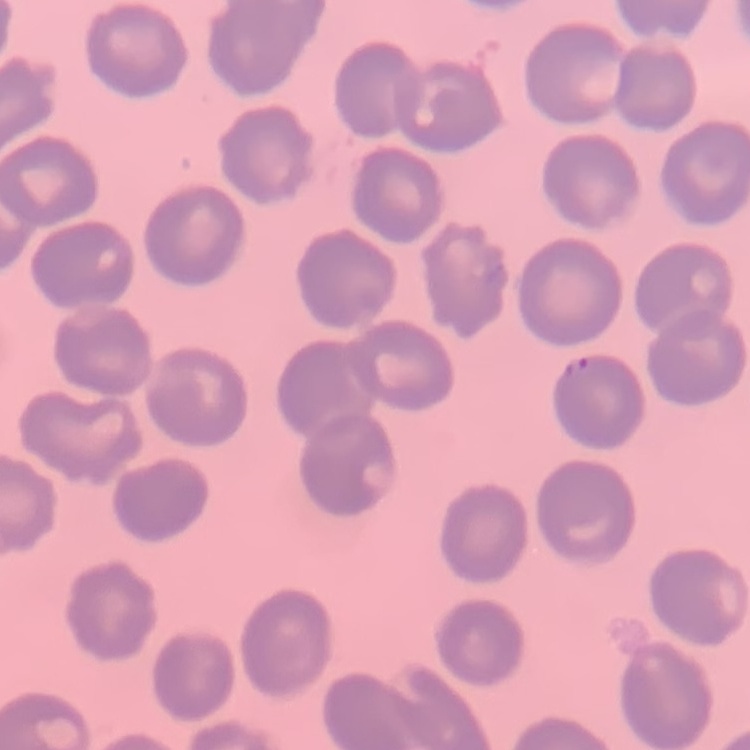

Summary:
  - Red blood cell morphology: no rouleaux formation
  - Preparation: thin blood smear
  - Stain: Field's or Giemsa
  - Image type: one tile cut from a larger photomicrograph